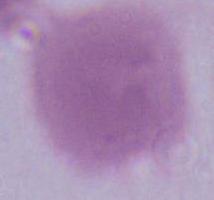

Summary:
  - Identification: red blood cell
  - Magnification: 1000x
  - Modality: photomicrograph